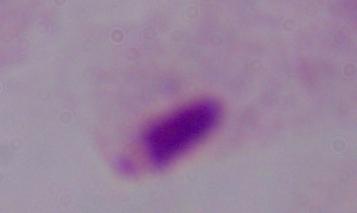
Summary:
  - Identification: trichomonad
  - Magnification: 1000x
  - Modality: photomicrograph